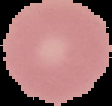

From a thin blood smear. Malaria status: uninfected. Image is 112×106 pixels. The area outside the segmented cell region is set to black.